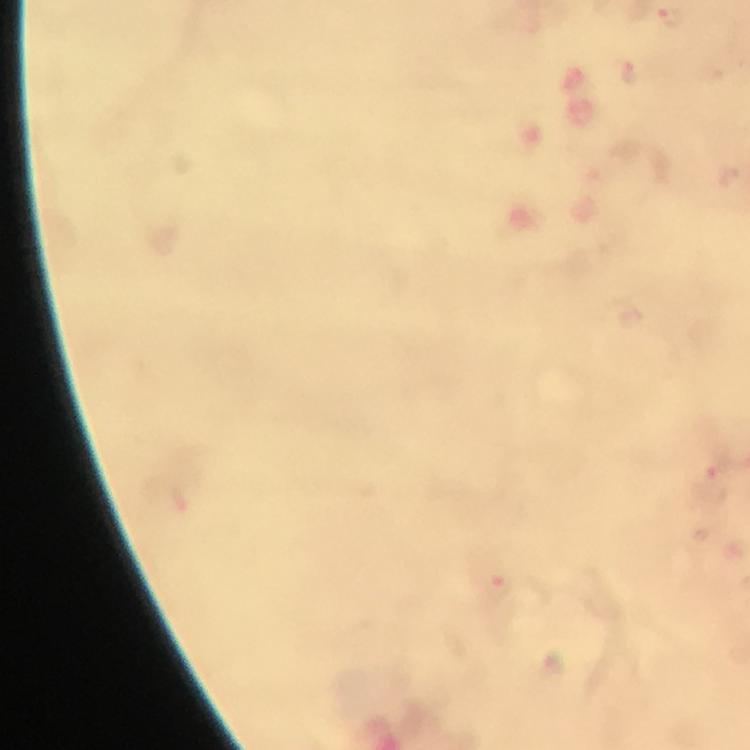

cropped from = a single field of view
magnification = 100x
immersion oil = used
capture = smartphone camera through the microscope
preparation = thick blood smear
context = from a diagnostic examination for malaria
Plasmodium parasite locations = approximate centers as (x, y) in pixels: (669, 16), (631, 69), (712, 479), (500, 586)
stain = Giemsa
image size = 750×750 pixels